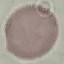

Summary:
  - Result: no malaria parasites detected
  - Preparation: thin blood film
  - Capture: smartphone camera at the microscope eyepiece
  - Stain: Giemsa
  - Image type: automatically extracted cell patch, resized to 64 × 64 pixels